Assess for malaria.
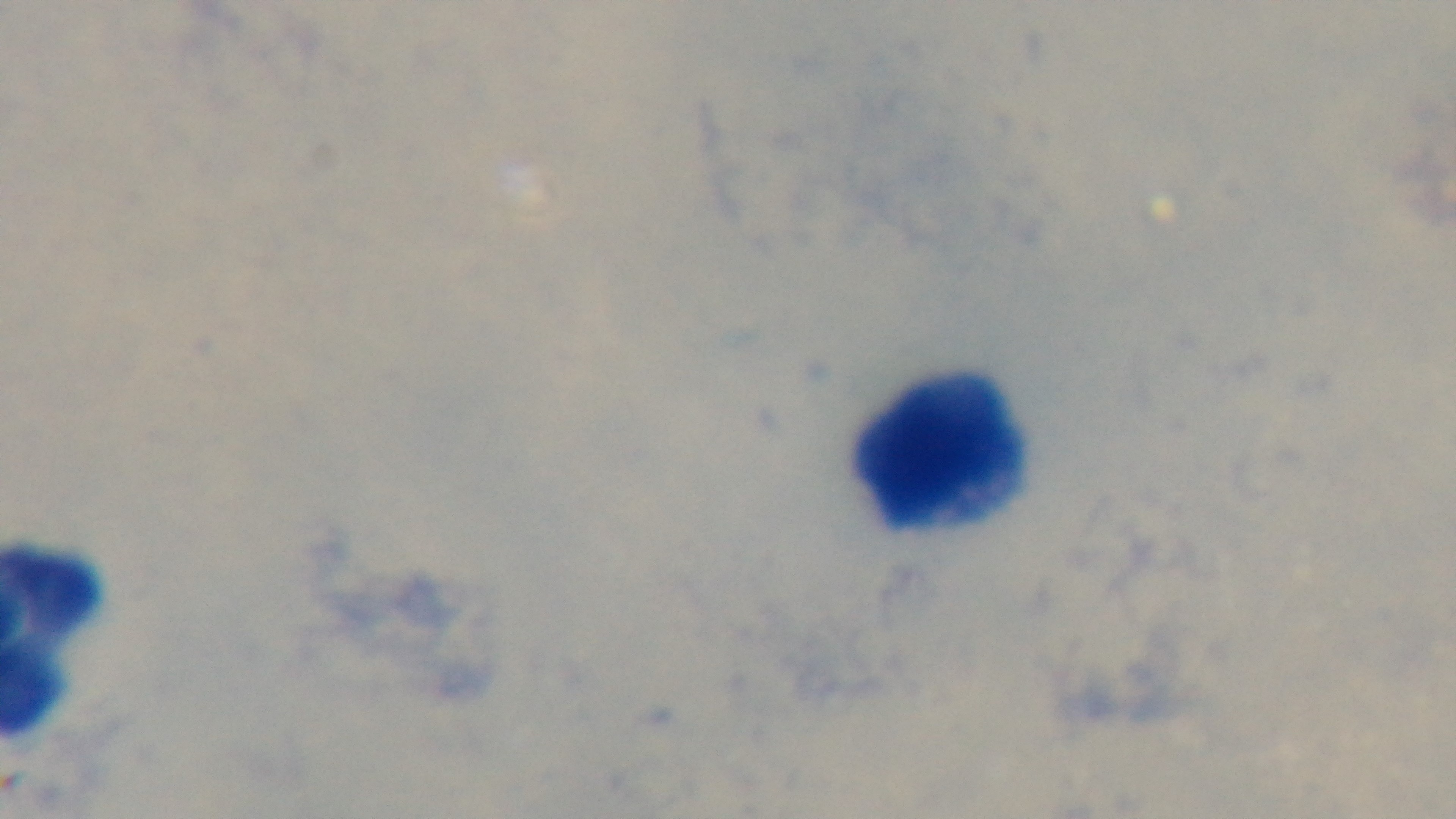

It is uninfected.

Summary:
  - Capture: mounted 4K digital camera
  - Stain: Giemsa
  - Field of view: single
  - Objective: 100x oil immersion
  - Preparation: thick blood film
  - Modality: light microscopy